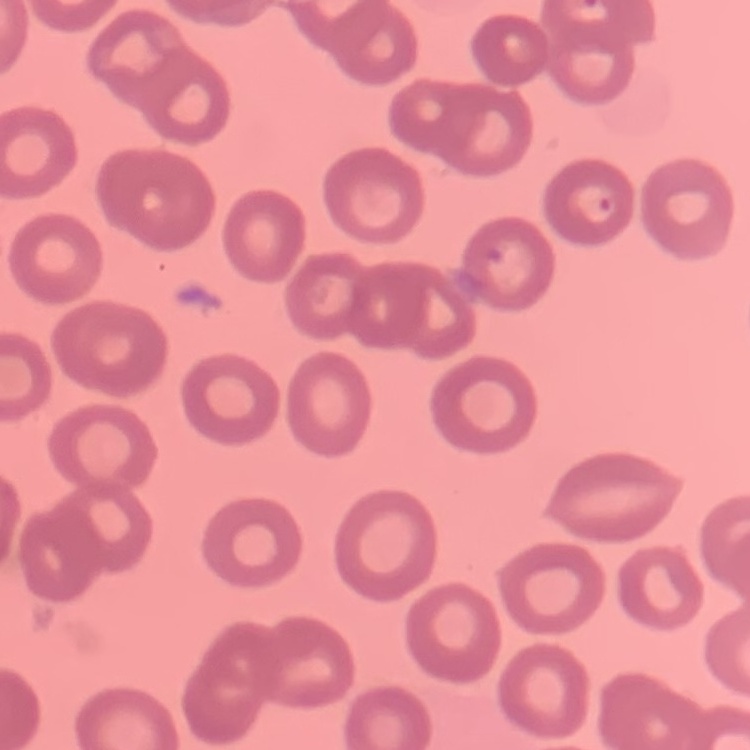

The red blood cells exhibit no rouleaux formation. Thin blood film. Field's or Giemsa stain. One tile cut from a larger photomicrograph.